Locate every Plasmodium falciparum parasite and identify its life-cycle stage.
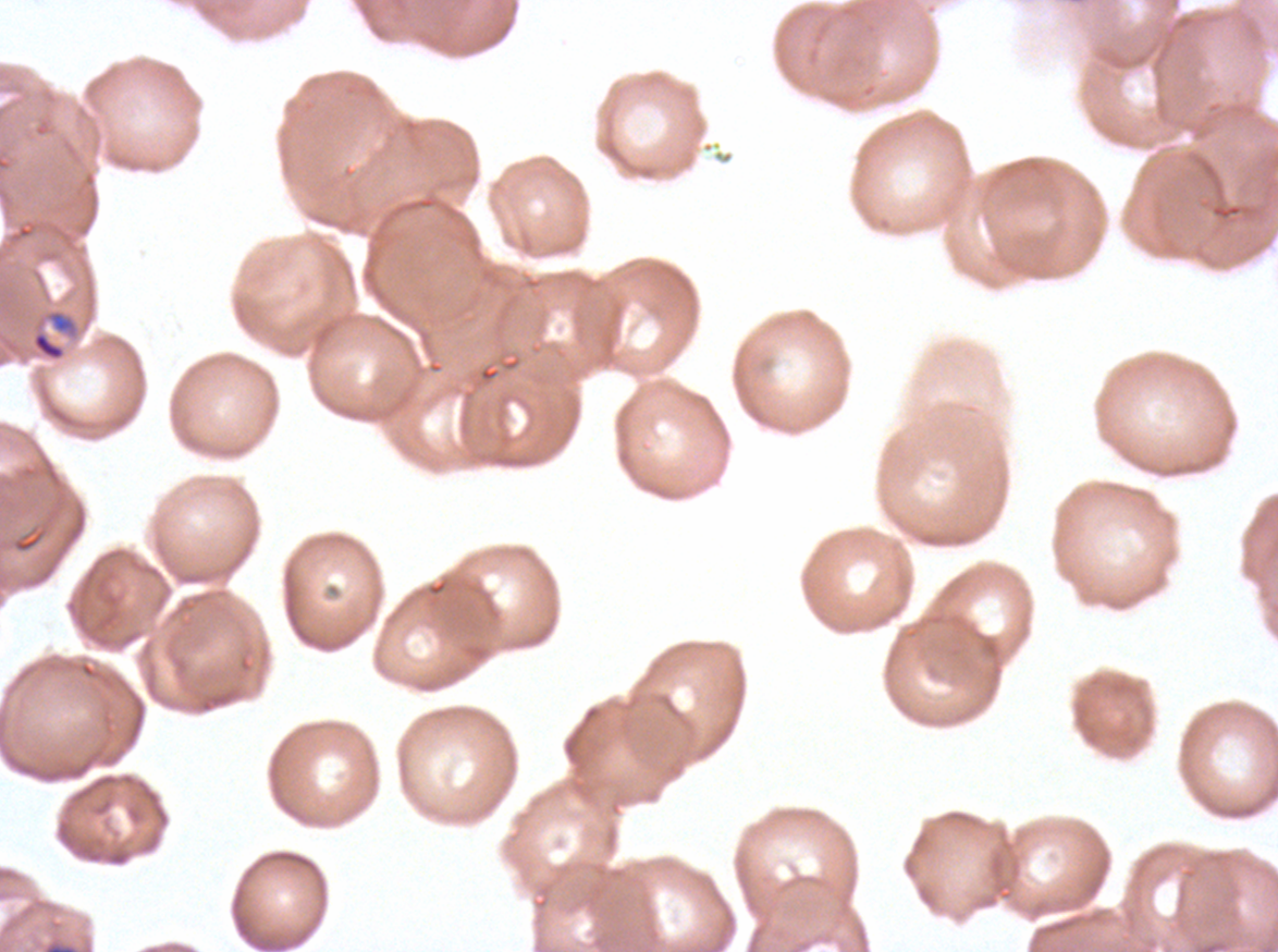

Approximate bounding rectangles given as corner coordinates in pixels from the top-left.
Late-ring/early-trophozoite forms: (x1=30, y1=307, x2=92, y2=363).
No rings, mid trophozoites, late trophozoites, early schizonts, late schizonts, segmenters, or gametocytes observed.

Plasmodium falciparum from a patient in The Gambia, cultured ex vivo for 24 to 48 hours. Giemsa stain. Image is 1278×952 pixels. One sub-image of a larger composite. Thin blood smear.